Report the malaria status of this cell.
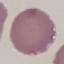
It is uninfected.

Automatically extracted cell patch, resized to 64 × 64 pixels. Giemsa stain. Thin smear of blood. Photographed with a smartphone camera at the microscope eyepiece.